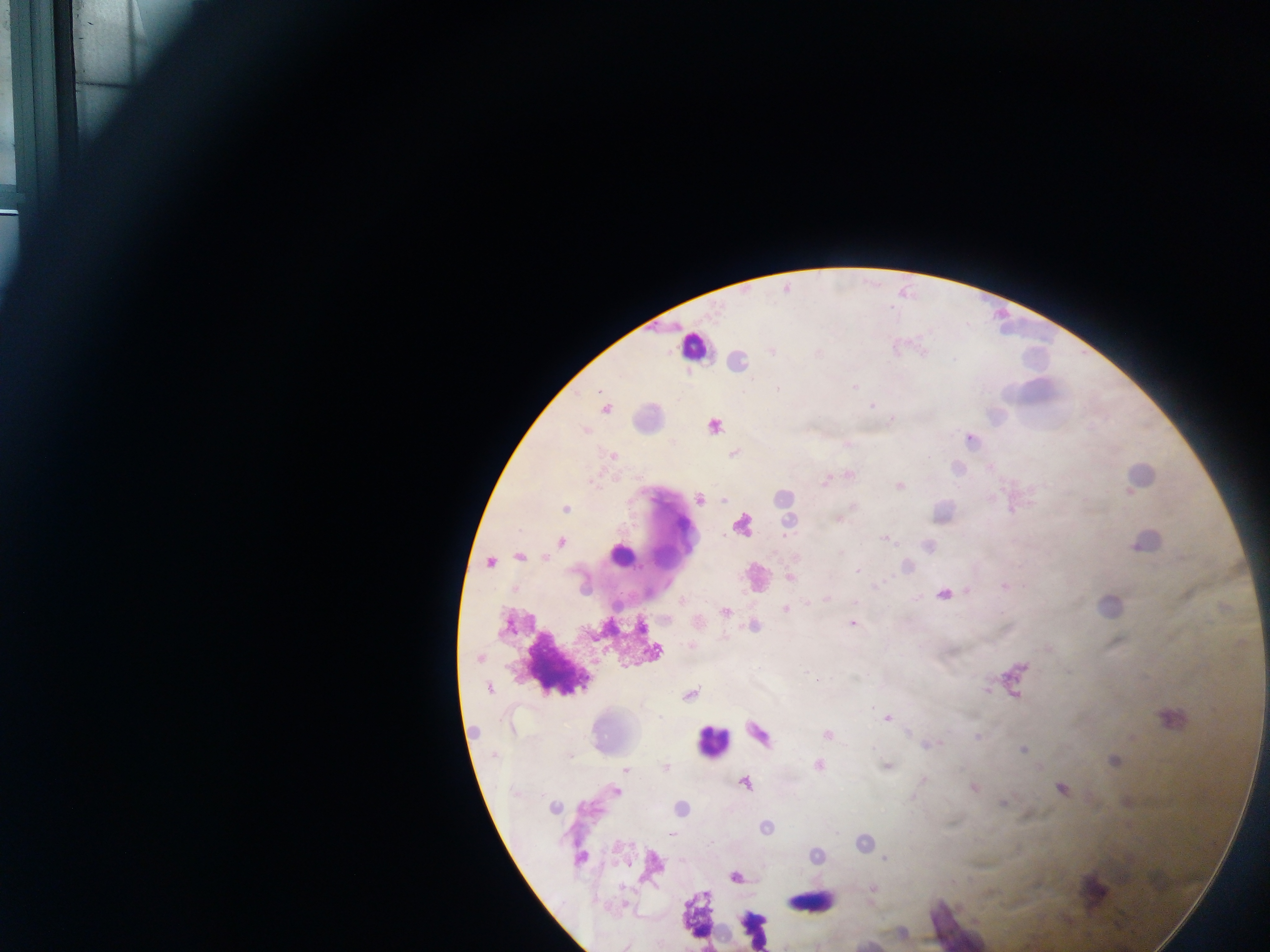

Approximate centers as (x, y) in pixels.
Summary:
  - Leukocyte locations: (695, 344), (745, 526), (666, 553), (618, 555), (758, 577), (711, 742), (1090, 893), (808, 901)
  - Malaria parasite locations: (772, 351), (854, 387), (777, 389), (872, 405), (605, 409), (714, 425), (584, 430), (733, 453), (613, 455), (825, 482), (899, 486), (700, 500), (725, 500), (566, 508), (885, 538), (561, 541), (519, 557), (490, 563), (857, 571), (790, 578), (1004, 586), (944, 595), (785, 608), (726, 612), (852, 623), (655, 651), (479, 658), (806, 672), (489, 689), (987, 690), (690, 695), (887, 718), (759, 733), (827, 735), (978, 737), (927, 745), (1023, 749), (570, 755), (819, 766), (666, 767), (887, 767), (626, 769), (924, 779), (745, 784), (973, 787), (1062, 788), (615, 791), (1004, 803), (554, 808), (681, 808), (766, 827), (671, 834), (885, 858), (580, 859), (734, 877), (625, 947)
  - Image size: 1270×952 pixels
  - Preparation: thick blood smear
  - Field of view: single
  - Capture: mobile-phone photograph through a microscope
  - Country: Ghana